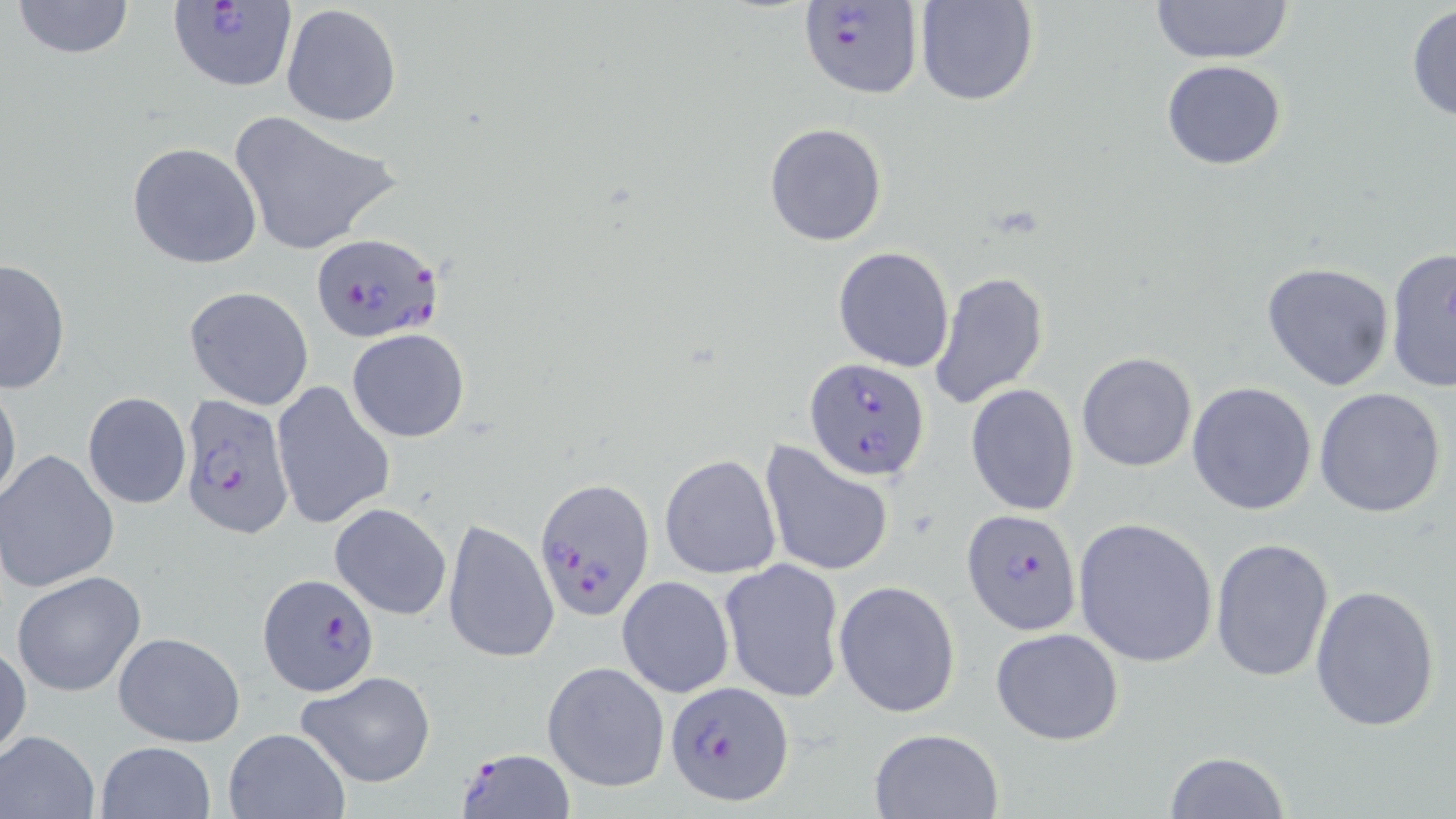
Approximate bounding boxes as [x1, y1, x2, y2] in pixels. Uninfected red blood cell locations: [11, 0, 137, 59], [916, 0, 1038, 106], [1149, 0, 1296, 65], [281, 5, 400, 128], [1406, 6, 1456, 122], [1161, 60, 1286, 169], [228, 113, 405, 257], [764, 122, 888, 247], [127, 141, 262, 269], [832, 246, 956, 372], [1385, 247, 1456, 393], [0, 257, 70, 395], [1262, 262, 1397, 392], [929, 270, 1049, 409], [184, 286, 315, 410], [345, 328, 471, 444], [1077, 352, 1197, 473], [0, 378, 21, 513], [269, 380, 396, 530], [1187, 382, 1317, 516], [965, 384, 1080, 516], [1313, 387, 1448, 518], [82, 392, 191, 509], [759, 440, 895, 579], [0, 449, 120, 593], [659, 455, 781, 579], [329, 502, 452, 620], [1073, 517, 1218, 667], [443, 518, 560, 666], [1209, 536, 1335, 685], [719, 558, 845, 702], [11, 570, 147, 698], [616, 575, 734, 697], [836, 581, 962, 718], [1310, 585, 1441, 732], [991, 628, 1124, 745], [113, 630, 245, 746], [0, 641, 30, 765], [543, 661, 671, 792], [295, 670, 438, 788], [223, 728, 349, 819], [868, 728, 1003, 818], [0, 729, 101, 818], [95, 740, 217, 819], [1163, 750, 1288, 818]. Plasmodium falciparum-infected red blood cell locations: [168, 1, 298, 96], [798, 1, 923, 99], [311, 235, 442, 344], [804, 358, 931, 482], [177, 391, 296, 539], [534, 477, 654, 621], [961, 509, 1082, 635], [256, 579, 376, 702], [666, 678, 792, 805], [453, 748, 579, 819]. Slide-level diagnosis: Plasmodium falciparum. One field of a larger specimen. May-Grünwald-Giemsa-stained preparation. 1000x magnification. Light microscopy. Thin blood smear. Image is 1456×819 pixels.